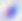
{
  "modality": "micrograph",
  "magnification": "400x",
  "identification": "Toxoplasma gondii"
}